Assess the morphology of the erythrocytes.
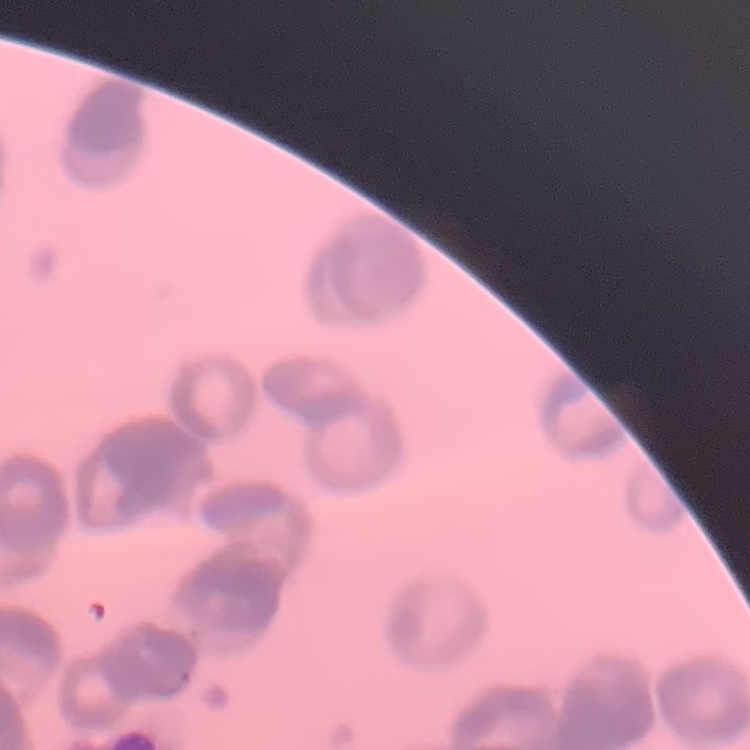

Rouleaux formation.

preparation = thin peripheral smear
image type = one tile cut from a larger photomicrograph
stain = Field's or Giemsa